Classify this cell by malaria status.
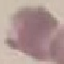
It is uninfected.

image_type: automatically extracted cell patch, resized to 64 × 64 pixels
capture: smartphone through the microscope eyepiece
stain: Giemsa
preparation: thin smear